Give the extent of all Trypanosoma brucei.
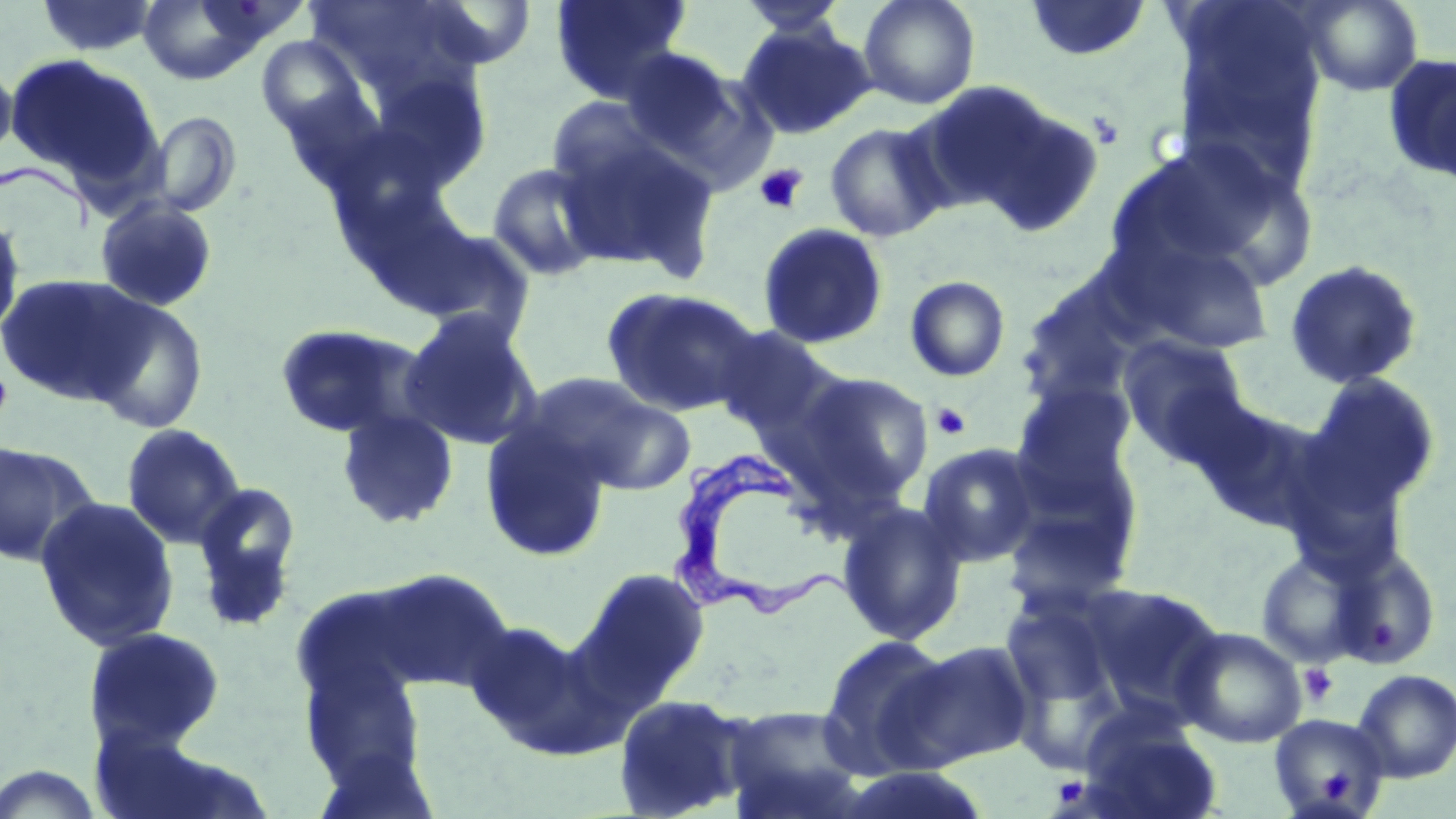

Approximate bounding boxes as named x1/y1/x2/y2 corners in pixels.
Trypanosoma brucei: (x1=674, y1=452, x2=856, y2=623).

Summary:
  - Uninfected red blood cell locations: (x1=37, y1=0, x2=157, y2=57), (x1=136, y1=0, x2=273, y2=85), (x1=550, y1=0, x2=692, y2=103), (x1=858, y1=0, x2=980, y2=110), (x1=1025, y1=0, x2=1152, y2=62), (x1=1168, y1=0, x2=1329, y2=189), (x1=1299, y1=0, x2=1424, y2=96), (x1=738, y1=1, x2=850, y2=38), (x1=735, y1=21, x2=876, y2=140), (x1=257, y1=35, x2=373, y2=149), (x1=618, y1=47, x2=742, y2=158), (x1=5, y1=53, x2=162, y2=188), (x1=1381, y1=53, x2=1456, y2=184), (x1=0, y1=55, x2=18, y2=168), (x1=935, y1=85, x2=1107, y2=238), (x1=544, y1=96, x2=667, y2=192), (x1=145, y1=110, x2=243, y2=218), (x1=824, y1=121, x2=950, y2=243), (x1=556, y1=131, x2=720, y2=277), (x1=1109, y1=137, x2=1300, y2=282), (x1=486, y1=161, x2=607, y2=282), (x1=94, y1=198, x2=218, y2=312), (x1=0, y1=209, x2=25, y2=343), (x1=756, y1=222, x2=888, y2=349), (x1=405, y1=223, x2=539, y2=345), (x1=1112, y1=234, x2=1277, y2=357), (x1=1283, y1=259, x2=1424, y2=391), (x1=0, y1=272, x2=156, y2=407), (x1=905, y1=275, x2=1011, y2=382), (x1=1016, y1=275, x2=1151, y2=405), (x1=602, y1=287, x2=762, y2=417), (x1=82, y1=296, x2=210, y2=433), (x1=399, y1=310, x2=543, y2=451), (x1=273, y1=323, x2=432, y2=440), (x1=713, y1=325, x2=839, y2=442), (x1=1117, y1=334, x2=1251, y2=464), (x1=790, y1=369, x2=935, y2=507), (x1=516, y1=372, x2=669, y2=489), (x1=1305, y1=372, x2=1441, y2=509), (x1=1013, y1=381, x2=1137, y2=498), (x1=575, y1=393, x2=697, y2=495), (x1=1188, y1=399, x2=1332, y2=534), (x1=336, y1=408, x2=460, y2=530), (x1=479, y1=420, x2=612, y2=563), (x1=121, y1=423, x2=246, y2=549), (x1=0, y1=441, x2=99, y2=568), (x1=918, y1=442, x2=1043, y2=567), (x1=192, y1=480, x2=302, y2=621), (x1=999, y1=491, x2=1140, y2=615), (x1=33, y1=496, x2=180, y2=652), (x1=837, y1=500, x2=969, y2=646), (x1=1330, y1=547, x2=1442, y2=671), (x1=1255, y1=549, x2=1368, y2=668), (x1=574, y1=566, x2=710, y2=702), (x1=371, y1=568, x2=516, y2=693), (x1=1075, y1=582, x2=1226, y2=721), (x1=998, y1=589, x2=1126, y2=716), (x1=463, y1=619, x2=599, y2=753), (x1=83, y1=626, x2=227, y2=752), (x1=1173, y1=626, x2=1307, y2=748), (x1=816, y1=632, x2=956, y2=779), (x1=895, y1=639, x2=1036, y2=768), (x1=1352, y1=668, x2=1456, y2=783), (x1=612, y1=692, x2=753, y2=818), (x1=721, y1=703, x2=869, y2=819), (x1=1077, y1=705, x2=1223, y2=819), (x1=1268, y1=714, x2=1391, y2=819)
  - Platelet locations: (x1=755, y1=165, x2=808, y2=214), (x1=1, y1=366, x2=13, y2=426), (x1=931, y1=402, x2=972, y2=440), (x1=1299, y1=663, x2=1339, y2=708), (x1=1319, y1=767, x2=1359, y2=805)
  - Slide-level diagnosis: Trypanosoma brucei
  - Field of view: single
  - Magnification: 1000x
  - Stain: May-Grünwald-Giemsa
  - Preparation: thin blood smear
  - Modality: light microscopy
  - Image size: 1456×819 pixels